Locate every Plasmodium parasite by life-cycle stage, and every leukocyte.
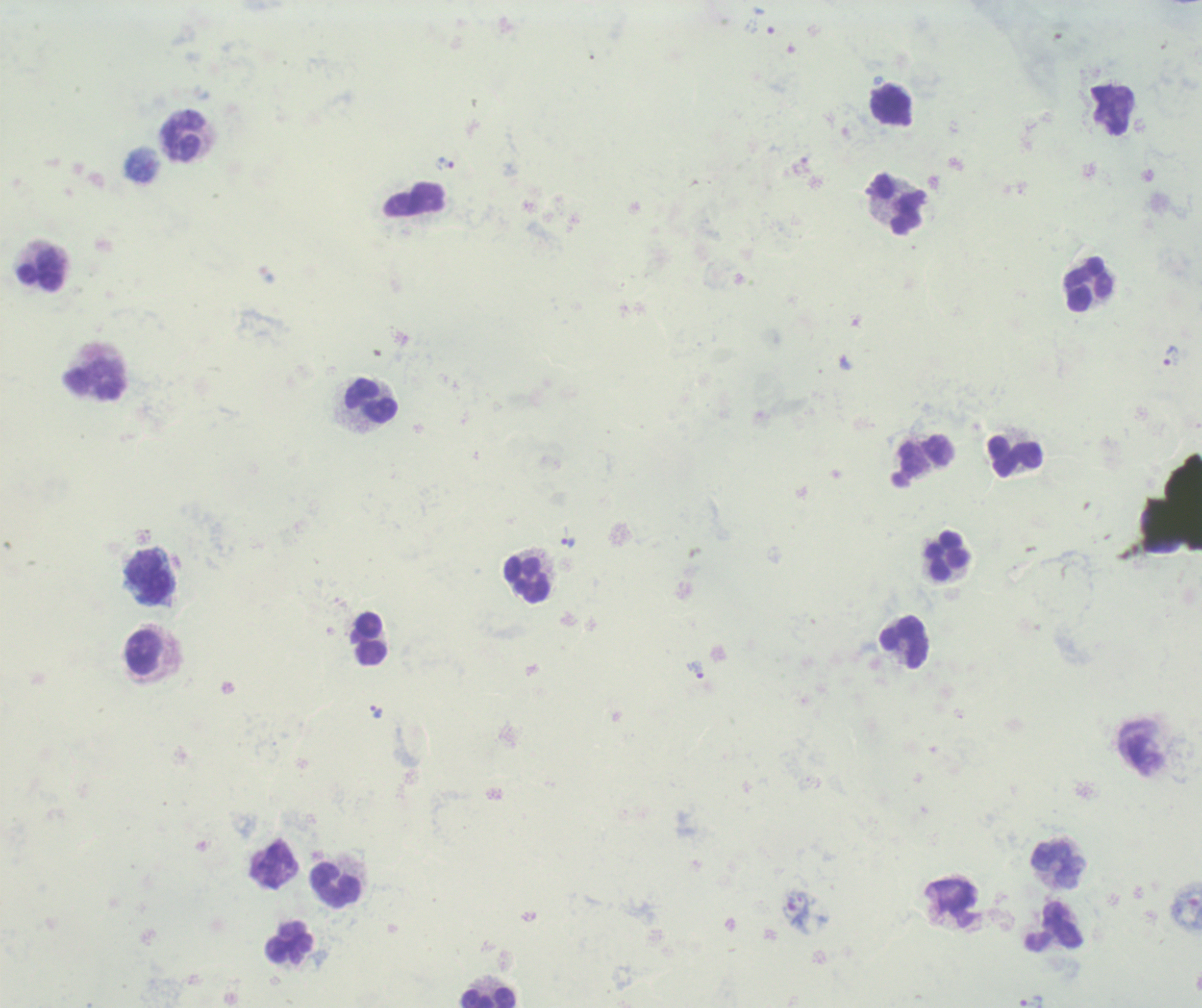
Approximate centers as [x, y] in pixels.
Trophozoites: [445, 163], [1172, 355], [567, 542], [697, 670], [377, 712], [1031, 1001].
No schizont or gametocyte forms observed.
Leukocytes: [891, 105], [183, 136], [415, 200], [898, 202], [41, 271], [1089, 284], [97, 379], [372, 400], [1014, 454], [927, 455], [948, 555], [149, 576], [527, 578], [370, 638], [904, 643], [143, 651], [1058, 865], [335, 885], [1054, 925], [289, 939], [486, 996].

Summary:
  - Magnification: 100x
  - Image size: 1202×1008 pixels
  - Preparation: thick blood film
  - Background quality: poor
  - Field of view: single
  - Context: previously used in an actual diagnosis
  - Stain: Romanowsky